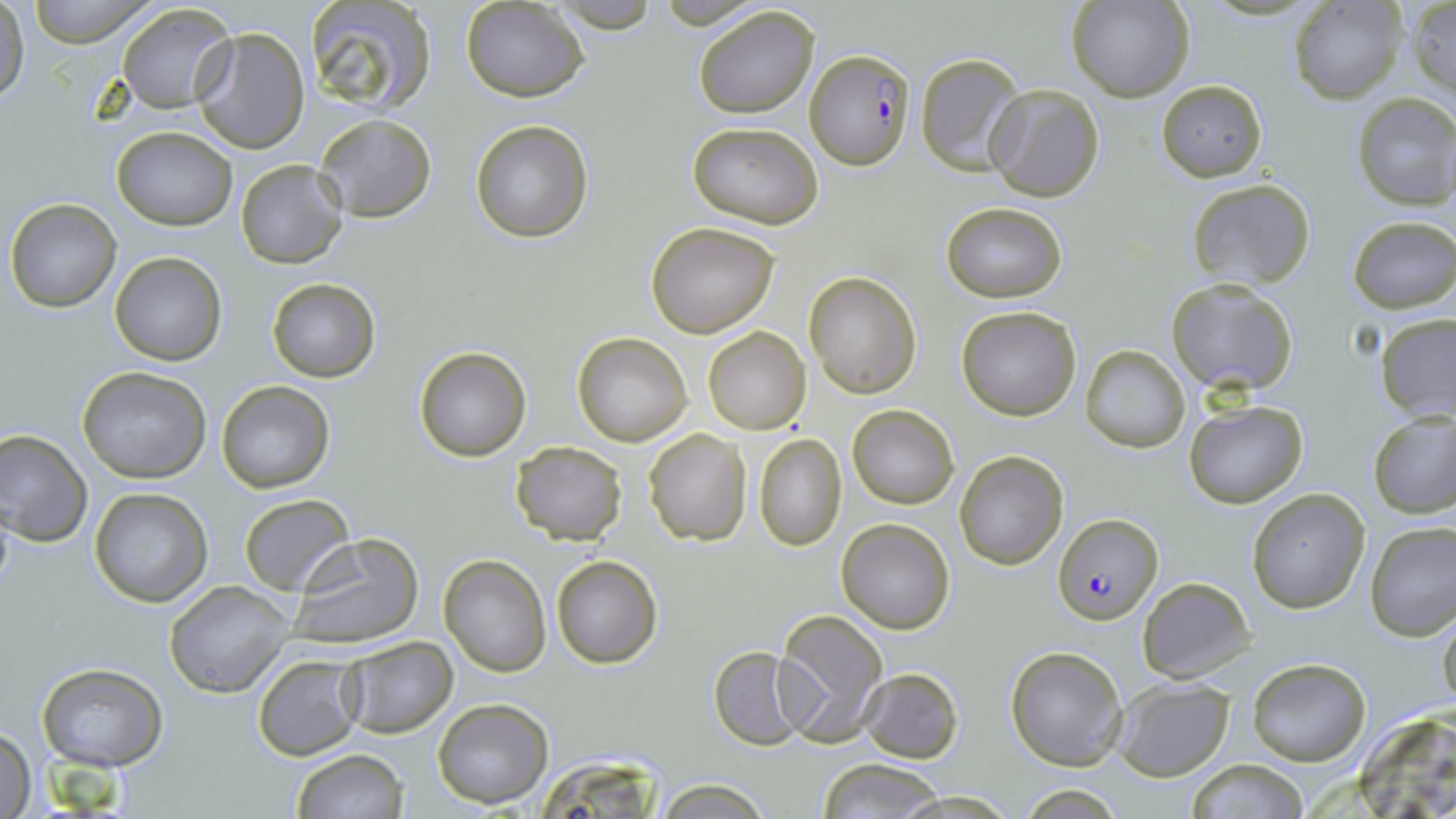
Summary:
  - Coordinate format: approximate bounding boxes as named x1/y1/x2/y2 corners in pixels
  - Uninfected red blood cell locations: (x1=20, y1=0, x2=160, y2=45), (x1=1068, y1=0, x2=1192, y2=102), (x1=1289, y1=0, x2=1406, y2=104), (x1=302, y1=1, x2=436, y2=117), (x1=548, y1=1, x2=662, y2=33), (x1=1407, y1=1, x2=1456, y2=100), (x1=0, y1=2, x2=28, y2=104), (x1=462, y1=2, x2=588, y2=101), (x1=117, y1=3, x2=237, y2=113), (x1=693, y1=5, x2=820, y2=117), (x1=191, y1=27, x2=311, y2=154), (x1=914, y1=53, x2=1025, y2=176), (x1=1155, y1=79, x2=1267, y2=181), (x1=985, y1=84, x2=1104, y2=202), (x1=1352, y1=93, x2=1456, y2=209), (x1=313, y1=115, x2=436, y2=221), (x1=471, y1=120, x2=593, y2=242), (x1=686, y1=122, x2=823, y2=230), (x1=111, y1=127, x2=237, y2=231), (x1=236, y1=160, x2=347, y2=268), (x1=1187, y1=179, x2=1316, y2=292), (x1=5, y1=199, x2=121, y2=312), (x1=942, y1=202, x2=1068, y2=302), (x1=1347, y1=216, x2=1456, y2=312), (x1=646, y1=220, x2=781, y2=337), (x1=110, y1=252, x2=227, y2=367), (x1=803, y1=272, x2=921, y2=398), (x1=265, y1=278, x2=381, y2=382), (x1=1165, y1=278, x2=1298, y2=395), (x1=956, y1=307, x2=1080, y2=421), (x1=1376, y1=314, x2=1456, y2=421), (x1=702, y1=325, x2=812, y2=435), (x1=571, y1=331, x2=692, y2=445), (x1=1081, y1=346, x2=1190, y2=452), (x1=413, y1=348, x2=530, y2=461), (x1=76, y1=366, x2=212, y2=482), (x1=216, y1=381, x2=336, y2=494), (x1=1182, y1=399, x2=1308, y2=508), (x1=847, y1=403, x2=959, y2=509), (x1=1367, y1=410, x2=1456, y2=518), (x1=644, y1=428, x2=753, y2=546), (x1=0, y1=429, x2=93, y2=547), (x1=753, y1=432, x2=847, y2=551), (x1=509, y1=440, x2=628, y2=546), (x1=954, y1=450, x2=1068, y2=570), (x1=90, y1=488, x2=213, y2=607), (x1=1246, y1=488, x2=1369, y2=612), (x1=239, y1=493, x2=353, y2=596), (x1=836, y1=518, x2=956, y2=634), (x1=1365, y1=521, x2=1456, y2=640), (x1=286, y1=532, x2=426, y2=650), (x1=439, y1=554, x2=552, y2=676), (x1=551, y1=555, x2=664, y2=670), (x1=1137, y1=577, x2=1254, y2=683), (x1=164, y1=581, x2=294, y2=697), (x1=771, y1=609, x2=888, y2=741), (x1=1437, y1=612, x2=1456, y2=711), (x1=338, y1=637, x2=458, y2=738), (x1=1005, y1=645, x2=1128, y2=769), (x1=709, y1=647, x2=809, y2=750), (x1=253, y1=654, x2=366, y2=761), (x1=1247, y1=657, x2=1371, y2=766), (x1=36, y1=661, x2=169, y2=772), (x1=859, y1=667, x2=963, y2=763), (x1=1113, y1=679, x2=1236, y2=781), (x1=433, y1=698, x2=553, y2=810), (x1=1, y1=726, x2=37, y2=817), (x1=291, y1=748, x2=409, y2=819), (x1=816, y1=759, x2=951, y2=818), (x1=1183, y1=759, x2=1312, y2=817), (x1=654, y1=779, x2=773, y2=818), (x1=886, y1=790, x2=1022, y2=819)
  - Plasmodium falciparum-infected red blood cell locations: (x1=805, y1=48, x2=915, y2=169), (x1=1055, y1=514, x2=1162, y2=627)
  - Slide-level diagnosis: Plasmodium falciparum
  - Preparation: thin blood film
  - Magnification: 1000x
  - Field of view: single
  - Modality: light microscopy
  - Image size: 1456×819 pixels
  - Stain: May-Grünwald-Giemsa